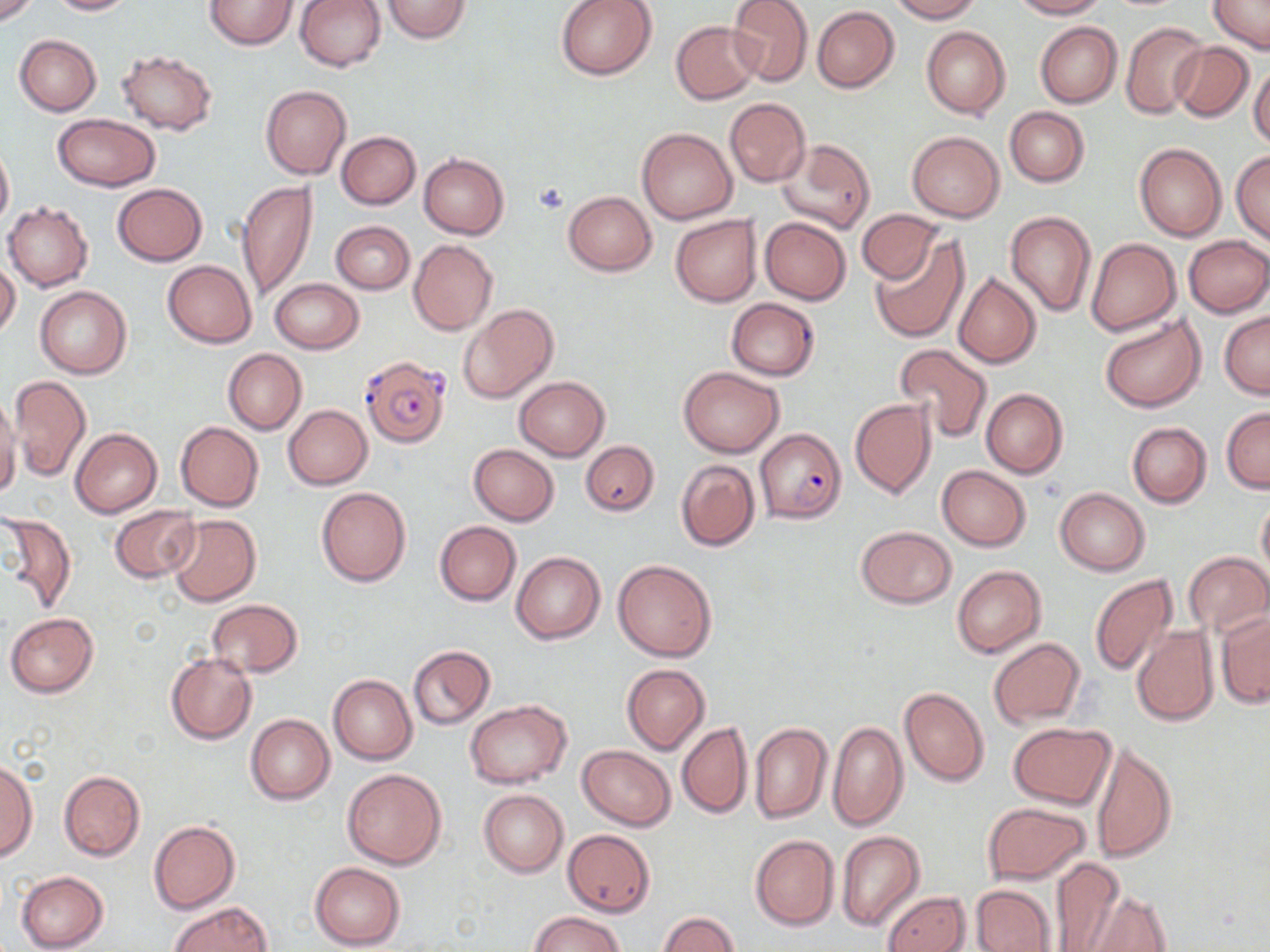
Approximate bounding boxes as (x1, y1, x2, y2) in pixels. Plasmodium falciparum-infected red blood cell locations: (360, 356, 450, 448), (754, 429, 846, 523). Uninfected red blood cell locations: (0, 0, 38, 26), (44, 0, 137, 15), (205, 0, 296, 49), (295, 0, 386, 72), (380, 0, 473, 46), (555, 0, 657, 80), (727, 0, 813, 87), (891, 0, 981, 23), (1008, 0, 1105, 19), (1208, 0, 1270, 53), (812, 6, 899, 92), (671, 20, 761, 104), (1035, 22, 1123, 107), (1121, 22, 1207, 119), (921, 26, 1009, 119), (14, 34, 102, 116), (1170, 41, 1254, 120), (115, 51, 218, 134), (1249, 61, 1270, 149), (260, 85, 351, 180), (724, 98, 810, 187), (1005, 107, 1089, 187), (51, 114, 160, 191), (636, 127, 737, 224), (337, 131, 420, 209), (907, 131, 1004, 222), (778, 139, 874, 235), (0, 142, 13, 233), (1134, 142, 1227, 243), (1232, 150, 1270, 245), (419, 153, 509, 239), (237, 181, 318, 304), (112, 183, 206, 265), (563, 191, 657, 275), (3, 202, 95, 292), (857, 209, 943, 284), (1006, 209, 1096, 317), (671, 215, 762, 307), (760, 217, 851, 305), (330, 221, 414, 294), (1183, 235, 1269, 317), (870, 238, 968, 343), (1086, 238, 1181, 337), (408, 240, 498, 336), (0, 259, 20, 340), (163, 259, 256, 347), (954, 272, 1041, 369), (271, 278, 363, 353), (34, 286, 131, 379), (726, 298, 819, 381), (458, 304, 558, 403), (1220, 311, 1270, 398), (1098, 312, 1207, 412), (894, 344, 992, 442), (223, 348, 306, 434), (678, 367, 784, 456), (8, 375, 90, 481), (514, 376, 610, 461), (980, 388, 1068, 478), (0, 393, 21, 505), (850, 398, 936, 499), (283, 405, 372, 490), (1221, 406, 1269, 492), (175, 422, 264, 511), (1127, 422, 1212, 508), (71, 428, 162, 517), (580, 439, 659, 515), (468, 444, 559, 525), (676, 459, 761, 551), (937, 466, 1029, 550), (315, 487, 411, 585), (1055, 487, 1151, 575), (1257, 496, 1270, 583), (109, 505, 201, 583), (1, 513, 78, 613), (166, 514, 261, 606), (434, 521, 520, 605), (856, 525, 956, 609), (1184, 551, 1269, 636), (512, 552, 605, 644), (612, 558, 717, 662), (952, 565, 1045, 658), (1088, 574, 1179, 677), (207, 599, 302, 678), (5, 613, 98, 697), (1217, 613, 1269, 708), (1131, 625, 1219, 727), (989, 637, 1086, 726), (408, 645, 495, 729), (165, 653, 257, 744), (622, 664, 710, 755), (328, 674, 418, 765), (899, 685, 990, 787), (464, 700, 571, 788), (245, 714, 335, 804), (750, 721, 832, 824), (677, 722, 752, 819), (827, 722, 908, 831), (1010, 722, 1115, 808), (1091, 742, 1177, 862), (577, 745, 676, 830), (0, 757, 37, 863), (341, 768, 447, 869), (59, 771, 145, 860), (478, 789, 569, 878), (982, 802, 1090, 883), (148, 820, 240, 915), (562, 830, 655, 917), (836, 831, 926, 932), (749, 835, 840, 931), (1048, 857, 1127, 952), (308, 862, 406, 951), (15, 872, 108, 951), (971, 883, 1058, 952), (1082, 890, 1171, 952), (882, 891, 969, 952), (168, 902, 271, 952), (529, 911, 627, 952), (658, 912, 739, 952). Platelet locations: (532, 183, 569, 214). Slide-level diagnosis: Plasmodium falciparum. Single field of view. 1000x magnification. May-Grünwald-Giemsa stain. Light microscopy. Thin blood smear. Image is 1270×952 pixels.